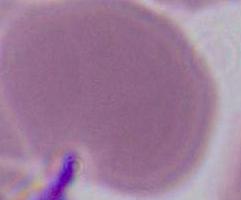
Summary:
  - Modality: micrograph
  - Identification: red blood cell
  - Magnification: 1000x